Outline each uninfected red blood cell.
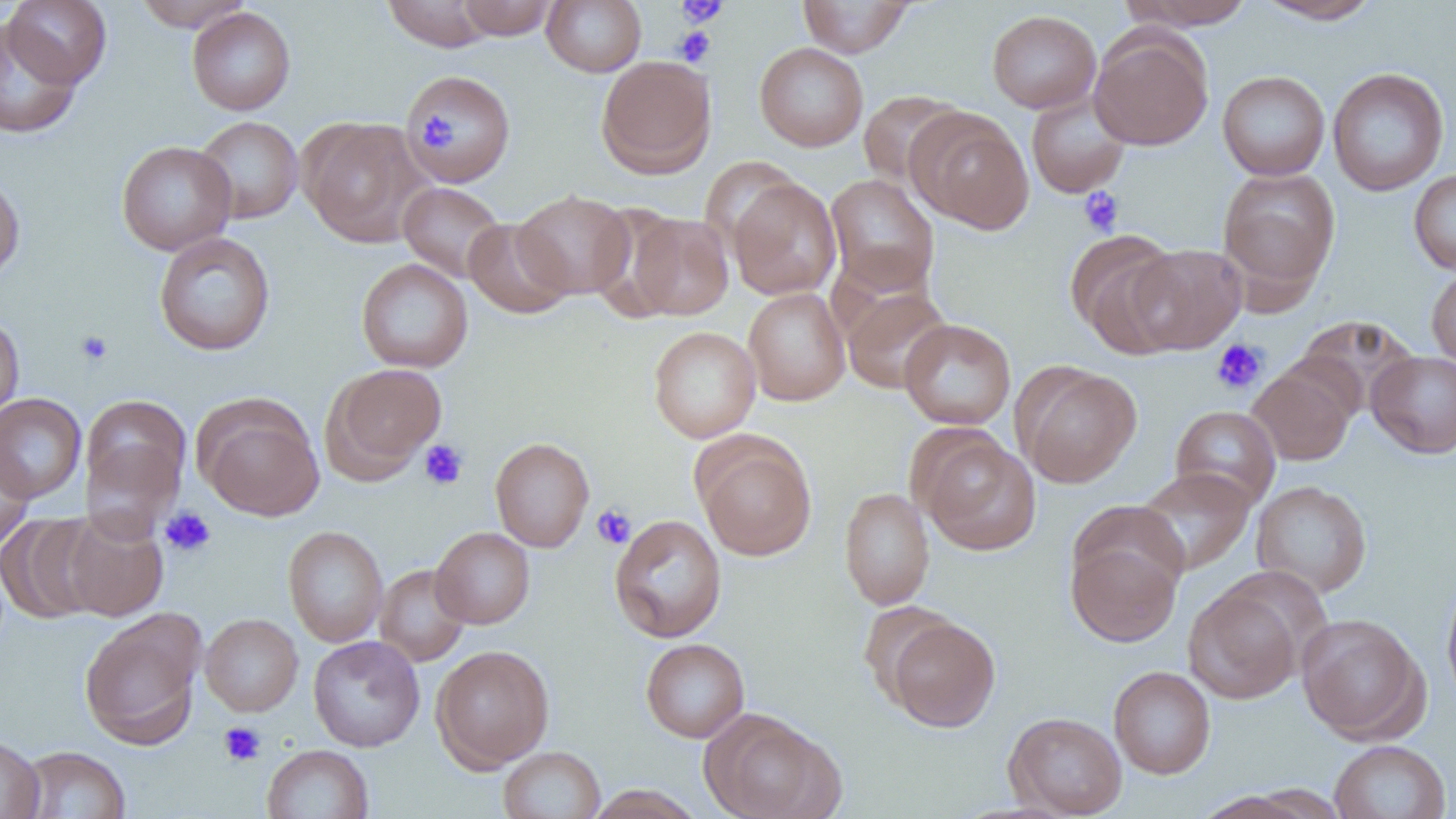

Approximate bounding boxes as (x1,y1)-(x2,y2) corner pairs in pixels.
Uninfected red blood cells: (3,0)-(112,88), (132,0)-(254,32), (382,0)-(498,52), (454,0)-(559,39), (542,0)-(646,76), (797,0)-(916,57), (1118,0)-(1257,29), (1253,0)-(1384,25), (186,6)-(296,115), (987,9)-(1101,113), (0,17)-(83,139), (1089,29)-(1214,150), (754,42)-(868,151), (596,55)-(716,179), (1326,67)-(1450,196), (403,69)-(516,186), (1217,70)-(1330,180), (858,90)-(965,189), (1025,92)-(1131,199), (908,109)-(1035,233), (193,116)-(304,223), (302,119)-(432,247), (116,140)-(237,256), (1217,166)-(1341,299), (1408,170)-(1456,275), (0,171)-(25,284), (825,174)-(939,296), (727,178)-(842,300), (398,181)-(507,282), (514,189)-(635,299), (627,212)-(734,320), (463,217)-(574,319), (1065,228)-(1185,358), (154,232)-(275,356), (1125,243)-(1246,354), (356,258)-(474,373), (1426,266)-(1456,370), (743,287)-(851,406), (842,287)-(953,394), (0,312)-(25,423), (1295,314)-(1422,416), (899,318)-(1016,430), (648,326)-(761,443), (1367,350)-(1456,459), (324,362)-(446,480), (1247,363)-(1357,466), (1018,364)-(1142,488), (0,393)-(87,504), (81,394)-(191,507), (197,398)-(325,521), (1170,405)-(1281,509), (915,431)-(1042,556), (490,436)-(594,552), (696,436)-(816,561), (80,438)-(184,542), (0,440)-(34,553), (1134,467)-(1255,575), (1251,480)-(1372,598), (839,487)-(935,610), (60,509)-(169,621), (0,512)-(104,625), (609,514)-(727,643), (283,525)-(388,647), (430,527)-(535,629), (1066,531)-(1184,647), (374,564)-(471,666), (1440,574)-(1456,709), (1184,583)-(1303,704), (860,600)-(957,704), (79,611)-(204,749), (200,613)-(303,716), (1295,613)-(1428,743), (884,616)-(1000,732), (308,636)-(425,751), (640,638)-(750,742), (431,644)-(555,771), (1108,666)-(1216,779), (700,709)-(843,819), (1004,711)-(1128,817), (0,734)-(44,819), (1329,739)-(1451,819), (262,744)-(374,819), (17,745)-(131,819), (498,746)-(605,819), (582,785)-(706,819).

slide-level diagnosis = no evidence of blood parasites
modality = optical microscopy
platelet locations = approximate bounding boxes as (x1,y1)-(x2,y2) corner pairs in pixels: (675,0)-(729,27), (675,11)-(719,44), (674,26)-(716,67), (418,112)-(459,151), (1079,187)-(1124,236), (76,330)-(113,367), (1211,339)-(1268,395), (419,439)-(468,490), (591,504)-(636,549), (160,506)-(216,557), (218,721)-(266,767)
preparation = thin blood film
image size = 1456×819 pixels
magnification = 1000x
field of view = one of a larger specimen